Identify the parasite.
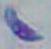
This is Toxoplasma gondii.

1000x magnification. Photomicrograph.